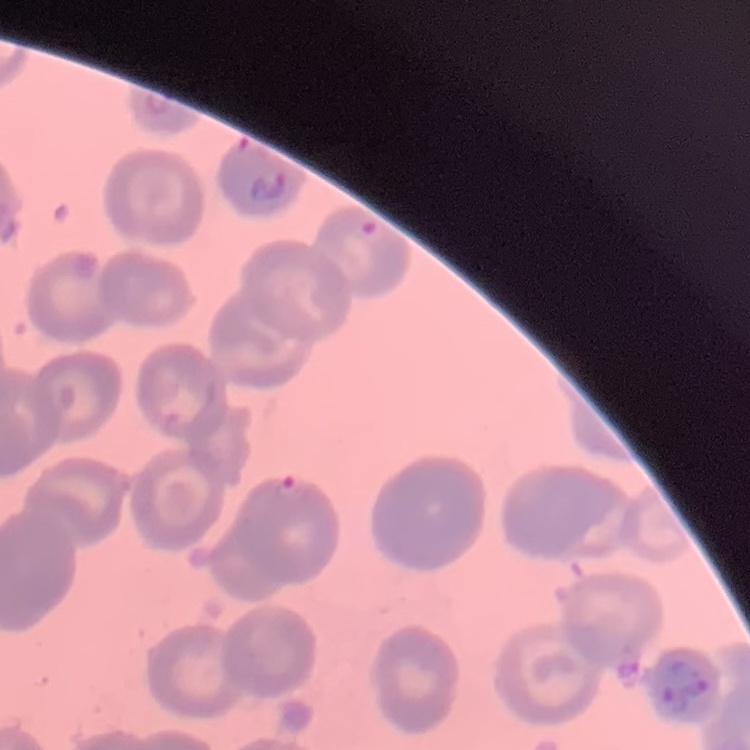

{
  "red_blood_cell_morphology": "no rouleaux formation",
  "preparation": "thin peripheral smear",
  "stain": "Field's or Giemsa",
  "image_type": "one tile cut from a larger photomicrograph"
}